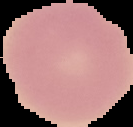

{
  "image_type": "cell region segmented out of the field of view; surrounding area masked to black",
  "preparation": "thin blood smear",
  "image_size": "133×127 pixels",
  "result": "no malaria parasites detected"
}